Give the position of every malaria parasite.
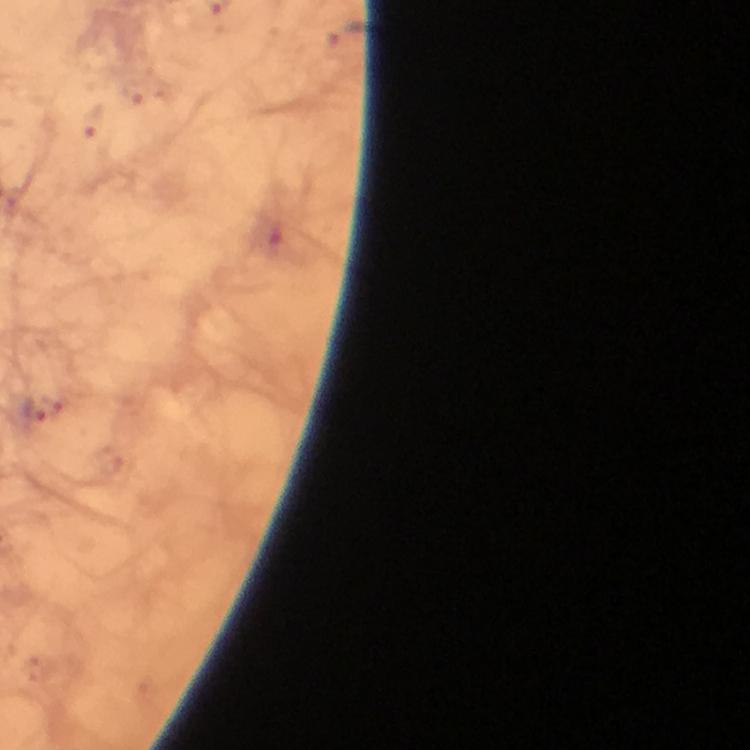
Approximate object centers, in pixels from the top-left corner.
Malaria parasites: (x=33, y=410).

Summary:
  - Preparation: thick blood film
  - Image size: 750×750 pixels
  - Stain: Giemsa
  - Magnification: 100x
  - Context: from a diagnostic examination for malaria
  - Capture: smartphone camera through the microscope
  - Immersion oil: applied
  - Cropped from: one field of view